Locate every blood parasite and identify its species.
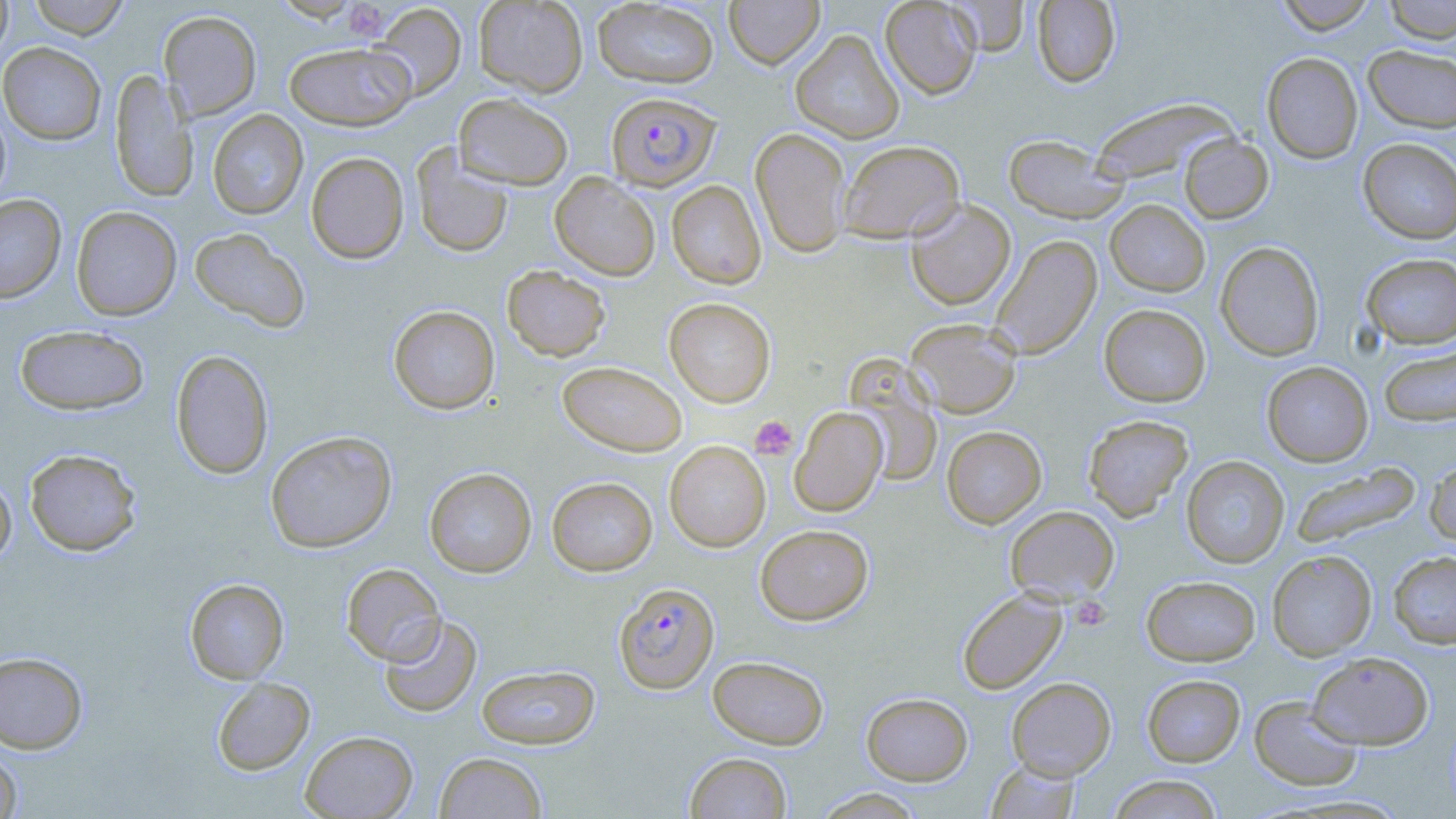

Approximate bounding boxes as named x1/y1/x2/y2 corners in pixels.
Plasmodium falciparum-infected red blood cells: (x1=606, y1=91, x2=720, y2=191), (x1=614, y1=582, x2=720, y2=694).
No Plasmodium ovale, Plasmodium malariae, Plasmodium vivax, Babesia divergens, or Trypanosoma brucei observed.

Summary:
  - Uninfected red blood cell locations: (x1=0, y1=0, x2=13, y2=61), (x1=28, y1=0, x2=129, y2=39), (x1=474, y1=0, x2=589, y2=97), (x1=593, y1=0, x2=719, y2=88), (x1=724, y1=0, x2=825, y2=69), (x1=880, y1=0, x2=982, y2=99), (x1=1032, y1=0, x2=1121, y2=87), (x1=1274, y1=0, x2=1379, y2=34), (x1=1382, y1=0, x2=1456, y2=43), (x1=947, y1=1, x2=1030, y2=55), (x1=371, y1=3, x2=467, y2=100), (x1=158, y1=10, x2=261, y2=120), (x1=790, y1=29, x2=904, y2=144), (x1=284, y1=41, x2=416, y2=130), (x1=0, y1=42, x2=106, y2=145), (x1=1363, y1=45, x2=1456, y2=133), (x1=1261, y1=52, x2=1363, y2=164), (x1=109, y1=69, x2=197, y2=204), (x1=453, y1=92, x2=574, y2=190), (x1=1091, y1=98, x2=1236, y2=186), (x1=0, y1=102, x2=12, y2=207), (x1=207, y1=109, x2=308, y2=220), (x1=750, y1=127, x2=852, y2=259), (x1=1003, y1=134, x2=1127, y2=224), (x1=1180, y1=134, x2=1273, y2=223), (x1=838, y1=139, x2=965, y2=242), (x1=1358, y1=139, x2=1456, y2=244), (x1=412, y1=145, x2=513, y2=258), (x1=306, y1=152, x2=409, y2=264), (x1=550, y1=172, x2=661, y2=281), (x1=667, y1=180, x2=767, y2=289), (x1=0, y1=194, x2=66, y2=303), (x1=905, y1=198, x2=1016, y2=311), (x1=1105, y1=200, x2=1210, y2=296), (x1=71, y1=206, x2=182, y2=320), (x1=189, y1=227, x2=311, y2=333), (x1=989, y1=234, x2=1102, y2=360), (x1=1215, y1=241, x2=1325, y2=361), (x1=1361, y1=253, x2=1456, y2=349), (x1=502, y1=265, x2=611, y2=361), (x1=665, y1=298, x2=776, y2=406), (x1=1099, y1=304, x2=1211, y2=407), (x1=388, y1=305, x2=500, y2=414), (x1=905, y1=318, x2=1022, y2=418), (x1=14, y1=324, x2=149, y2=415), (x1=1379, y1=345, x2=1455, y2=428), (x1=170, y1=349, x2=274, y2=479), (x1=845, y1=356, x2=942, y2=487), (x1=558, y1=361, x2=687, y2=456), (x1=1261, y1=361, x2=1373, y2=466), (x1=790, y1=406, x2=887, y2=516), (x1=1083, y1=414, x2=1194, y2=520), (x1=941, y1=425, x2=1047, y2=528), (x1=265, y1=431, x2=397, y2=553), (x1=664, y1=441, x2=770, y2=552), (x1=24, y1=448, x2=142, y2=556), (x1=1181, y1=456, x2=1289, y2=568), (x1=1425, y1=456, x2=1456, y2=548), (x1=1290, y1=461, x2=1422, y2=548), (x1=424, y1=467, x2=536, y2=577), (x1=0, y1=473, x2=16, y2=569), (x1=547, y1=476, x2=657, y2=576), (x1=1005, y1=505, x2=1119, y2=603), (x1=755, y1=524, x2=873, y2=624), (x1=1267, y1=550, x2=1377, y2=660), (x1=1388, y1=550, x2=1456, y2=648), (x1=341, y1=563, x2=446, y2=666), (x1=1141, y1=576, x2=1260, y2=666), (x1=185, y1=578, x2=289, y2=683), (x1=956, y1=588, x2=1067, y2=694), (x1=379, y1=614, x2=482, y2=718), (x1=0, y1=651, x2=89, y2=753), (x1=1308, y1=651, x2=1433, y2=750), (x1=707, y1=655, x2=829, y2=749), (x1=476, y1=664, x2=601, y2=749), (x1=1142, y1=674, x2=1245, y2=767), (x1=212, y1=677, x2=315, y2=775), (x1=1006, y1=677, x2=1116, y2=780), (x1=861, y1=692, x2=973, y2=785), (x1=1249, y1=696, x2=1364, y2=791), (x1=300, y1=730, x2=418, y2=818), (x1=0, y1=745, x2=22, y2=819), (x1=434, y1=751, x2=547, y2=818), (x1=684, y1=751, x2=792, y2=818), (x1=986, y1=760, x2=1081, y2=818), (x1=1108, y1=774, x2=1223, y2=818), (x1=812, y1=788, x2=929, y2=818)
  - Platelet locations: (x1=340, y1=0, x2=385, y2=44), (x1=750, y1=415, x2=798, y2=460), (x1=1070, y1=596, x2=1111, y2=631)
  - Slide-level diagnosis: Plasmodium falciparum
  - Preparation: thin blood film
  - Image size: 1456×819 pixels
  - Field of view: one of a larger specimen
  - Stain: May-Grünwald-Giemsa
  - Magnification: 1000x
  - Modality: light microscopy